Classify this cell by malaria status.
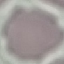

Uninfected.

Photographed with a smartphone camera at the microscope eyepiece. Automatically extracted cell patch, resized to 64 × 64 pixels. Thin blood smear. Giemsa stain.